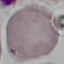 Result: no malaria parasites detected. Giemsa stain. Acquired by smartphone through the microscope eyepiece. Automatically extracted cell patch, resized to 64 × 64 pixels. Thin blood film.